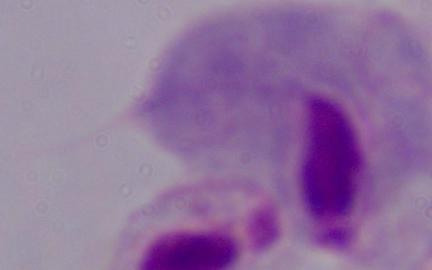

Summary:
  - Identification: trichomonad
  - Modality: micrograph
  - Magnification: 1000x